Name the cell type shown.
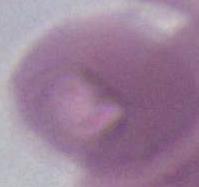
This is an erythrocyte.

Micrograph. 1000x magnification.